Identify the parasite.
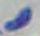
This is Toxoplasma gondii.

Summary:
  - Magnification: 1000x
  - Modality: photomicrograph